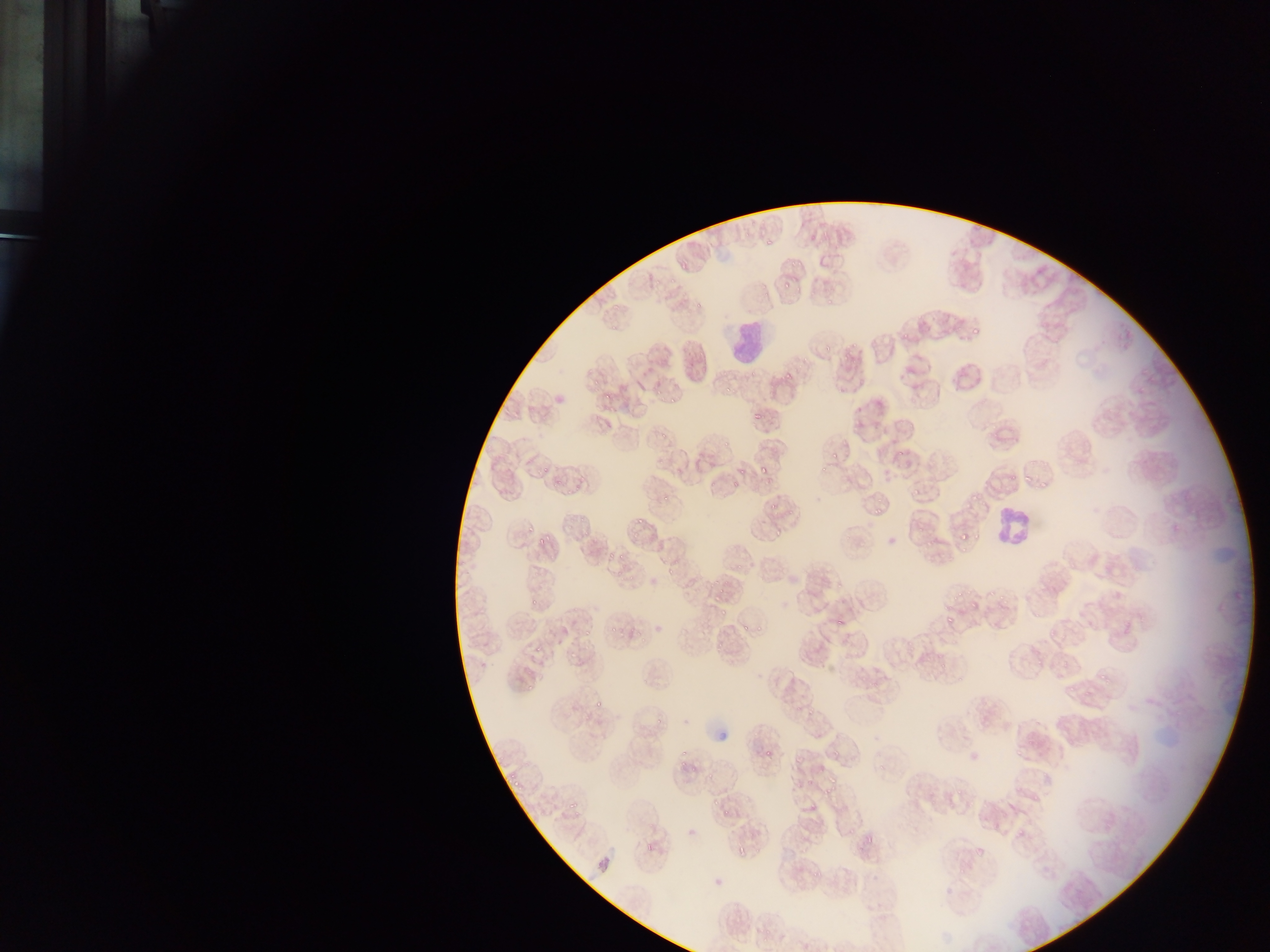
Approximate bounding boxes as [left, top, right, bottom] in pixels.
Summary:
  - Leukocyte locations: [727, 321, 766, 359], [996, 502, 1041, 554]
  - Malaria parasite locations: [764, 235, 778, 245], [788, 259, 801, 272], [681, 263, 688, 274], [784, 278, 789, 293], [668, 279, 677, 288], [822, 295, 832, 306], [694, 303, 701, 316], [971, 323, 984, 338], [898, 333, 908, 344], [819, 344, 832, 356], [784, 367, 796, 380], [587, 377, 601, 387], [618, 382, 628, 393], [720, 386, 735, 396], [651, 387, 665, 398], [600, 392, 611, 402], [667, 396, 677, 408], [750, 409, 765, 428], [655, 419, 674, 434], [721, 441, 731, 453], [828, 448, 840, 463], [539, 465, 550, 476], [734, 467, 745, 474], [758, 467, 767, 477], [1008, 473, 1018, 482], [1021, 475, 1030, 488], [552, 477, 566, 491], [1039, 482, 1045, 491], [729, 483, 740, 492], [967, 486, 983, 501], [662, 489, 671, 506], [910, 489, 919, 501], [769, 501, 780, 512], [871, 508, 881, 520], [634, 513, 645, 527], [525, 521, 538, 534], [537, 525, 556, 548], [772, 529, 785, 542], [958, 533, 972, 542], [923, 534, 941, 551], [605, 546, 619, 560], [618, 553, 625, 563], [663, 566, 677, 584], [716, 582, 728, 597], [990, 587, 997, 598], [1000, 587, 1013, 606], [954, 593, 961, 605], [529, 599, 544, 603], [475, 600, 489, 618], [719, 603, 731, 621], [754, 617, 768, 638], [835, 619, 846, 630], [946, 619, 954, 622], [606, 623, 619, 634], [737, 623, 748, 633], [581, 628, 591, 634], [713, 639, 727, 648], [532, 644, 541, 653], [566, 652, 577, 668], [1098, 670, 1108, 685], [1079, 681, 1094, 698], [524, 683, 539, 694], [593, 698, 605, 707], [805, 708, 814, 719], [650, 709, 667, 733], [677, 747, 695, 769], [762, 748, 774, 759], [690, 754, 704, 775], [508, 765, 527, 789], [824, 772, 835, 786], [954, 783, 968, 796], [821, 788, 833, 798], [709, 798, 720, 807], [568, 799, 579, 811], [720, 802, 735, 816], [1014, 819, 1029, 838], [862, 826, 878, 845], [737, 848, 745, 860], [972, 850, 982, 860], [811, 864, 830, 881] | approximate [x, y] pixel centers of objects too small to bound: [822, 470], [972, 606]
  - Image size: 1270×952 pixels
  - Preparation: thin blood film
  - Field of view: single
  - Capture: mobile-phone photograph through a microscope
  - Country: Ghana